Report the malaria status of this cell.
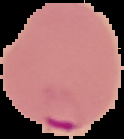

It is parasitized.

image type = cell region segmented out of the field of view; surrounding area masked to black
image size = 124×139 pixels
preparation = thin blood film